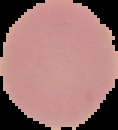

Image is 118×130 pixels. Malaria status: uninfected. The area outside the segmented cell region is set to black. From a thin blood smear.